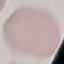

Summary:
  - Malaria status: uninfected
  - Preparation: thin blood smear
  - Image type: automatically extracted cell patch, resized to 64 × 64 pixels
  - Capture: smartphone camera at the microscope eyepiece
  - Stain: Giemsa